Comment on the morphology of the erythrocytes.
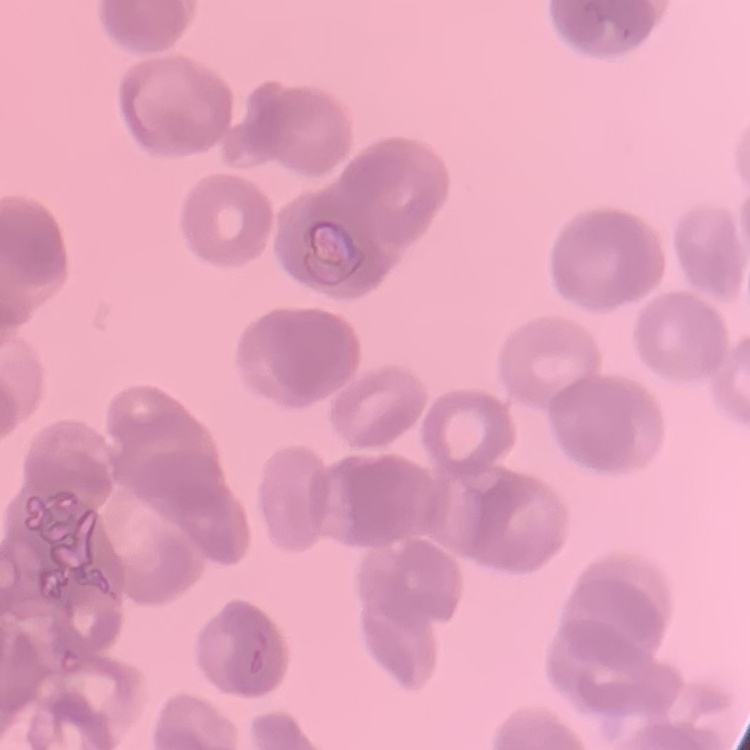
They show rouleaux formation.

stain = Field's or Giemsa
image type = square crop of a larger photomicrograph
preparation = thin blood film